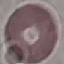

Malaria status: uninfected. Photographed with a smartphone camera at the microscope eyepiece. Giemsa-stained preparation. Cell patch, automatically extracted from a larger field of view and resized to 64 × 64 pixels. Thin blood film.